Point out each Plasmodium parasite and each leukocyte.
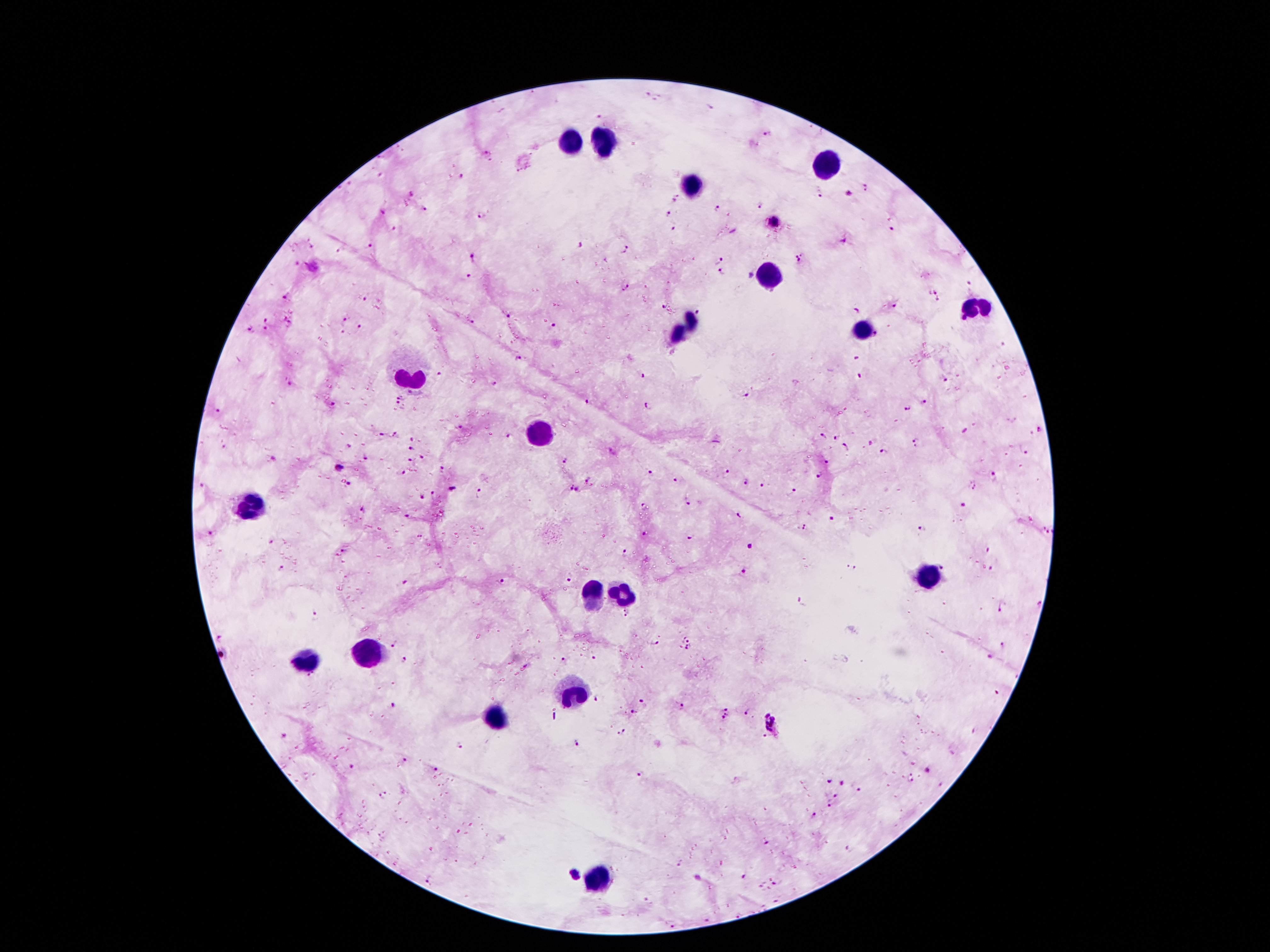

Approximate object centers, in pixels from the top-left corner.
Plasmodium parasites: (x=648, y=95), (x=712, y=108), (x=598, y=116), (x=768, y=133), (x=486, y=152), (x=379, y=174), (x=460, y=176), (x=868, y=187), (x=850, y=193), (x=412, y=194), (x=820, y=194), (x=673, y=198), (x=759, y=205), (x=719, y=207), (x=426, y=210), (x=382, y=211), (x=668, y=214), (x=482, y=215), (x=773, y=222), (x=393, y=229), (x=674, y=229), (x=893, y=230), (x=843, y=240), (x=311, y=243), (x=370, y=245), (x=580, y=245), (x=625, y=248), (x=338, y=250), (x=473, y=255), (x=800, y=258), (x=719, y=260), (x=723, y=273), (x=469, y=275), (x=968, y=283), (x=625, y=288), (x=936, y=291), (x=286, y=298), (x=363, y=299), (x=938, y=300), (x=663, y=306), (x=895, y=307), (x=858, y=310), (x=699, y=312), (x=507, y=318), (x=266, y=319), (x=344, y=320), (x=473, y=322), (x=554, y=326), (x=251, y=328), (x=360, y=328), (x=266, y=329), (x=344, y=333), (x=877, y=335), (x=1002, y=345), (x=518, y=358), (x=855, y=359), (x=646, y=375), (x=439, y=376), (x=860, y=376), (x=943, y=380), (x=290, y=384), (x=494, y=385), (x=413, y=393), (x=745, y=394), (x=403, y=396), (x=585, y=401), (x=926, y=403), (x=333, y=405), (x=398, y=405), (x=647, y=406), (x=907, y=407), (x=217, y=411), (x=462, y=427), (x=1039, y=429), (x=965, y=430), (x=396, y=434), (x=380, y=436), (x=507, y=436), (x=823, y=436), (x=833, y=437), (x=414, y=439), (x=916, y=442), (x=870, y=444), (x=348, y=446), (x=845, y=446), (x=412, y=448), (x=885, y=452), (x=1027, y=454), (x=565, y=457), (x=423, y=458), (x=367, y=460), (x=411, y=460), (x=829, y=462), (x=339, y=467), (x=446, y=469), (x=402, y=473), (x=650, y=473), (x=727, y=473), (x=995, y=476), (x=819, y=477), (x=590, y=480), (x=678, y=480), (x=746, y=481), (x=202, y=484), (x=349, y=484), (x=764, y=484), (x=972, y=485), (x=453, y=489), (x=574, y=489), (x=793, y=490), (x=432, y=493), (x=480, y=494), (x=422, y=497), (x=688, y=505), (x=964, y=506), (x=644, y=507), (x=364, y=510), (x=741, y=514), (x=406, y=515), (x=830, y=519), (x=805, y=527), (x=922, y=529), (x=1049, y=532), (x=210, y=533), (x=646, y=534), (x=419, y=536), (x=689, y=537), (x=270, y=542), (x=747, y=544), (x=343, y=551), (x=989, y=552), (x=626, y=554), (x=851, y=567), (x=943, y=567), (x=991, y=568), (x=280, y=569), (x=745, y=571), (x=571, y=577), (x=502, y=581), (x=405, y=582), (x=801, y=602), (x=1039, y=604), (x=1001, y=610), (x=628, y=612), (x=317, y=617), (x=222, y=635), (x=391, y=643), (x=688, y=643), (x=655, y=644), (x=1004, y=646), (x=223, y=654), (x=593, y=656), (x=562, y=660), (x=990, y=660), (x=403, y=661), (x=996, y=693), (x=597, y=699), (x=644, y=702), (x=396, y=705), (x=683, y=707), (x=633, y=713), (x=747, y=713), (x=726, y=715), (x=777, y=724), (x=622, y=732), (x=287, y=738), (x=459, y=743), (x=579, y=743), (x=403, y=760), (x=349, y=766), (x=437, y=770), (x=928, y=772), (x=641, y=773), (x=912, y=778), (x=829, y=782), (x=841, y=784), (x=383, y=793), (x=837, y=795), (x=830, y=807), (x=812, y=817), (x=767, y=845), (x=679, y=864), (x=576, y=876), (x=745, y=877), (x=432, y=880), (x=777, y=883), (x=761, y=885), (x=648, y=901), (x=739, y=914), (x=707, y=920), (x=675, y=926).
Leukocytes: (x=564, y=140), (x=606, y=143), (x=833, y=168), (x=690, y=186), (x=770, y=276), (x=978, y=309), (x=686, y=327), (x=860, y=327), (x=411, y=377), (x=545, y=433), (x=253, y=508), (x=928, y=577), (x=589, y=592), (x=623, y=596), (x=372, y=655), (x=308, y=663), (x=574, y=695), (x=495, y=717), (x=597, y=880).

Single field of view. 100x magnification. Image is 1270×952 pixels. Smartphone photograph taken through the microscope eyepiece. Patient malaria status: positive for Plasmodium falciparum. Giemsa stain. Thick blood film.